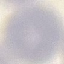
Malaria status: uninfected. Photographed with a smartphone camera at the microscope eyepiece. Thin blood film. Cell patch, automatically extracted from a larger field of view and resized to 64 × 64 pixels. Giemsa stain.